Assess this cell for malaria.
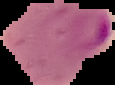

It is parasitized.

{
  "image_size": "115×85 pixels",
  "preparation": "thin blood smear",
  "image_type": "segmented cell region with the area outside set to black"
}